Give the position of every Plasmodium parasite.
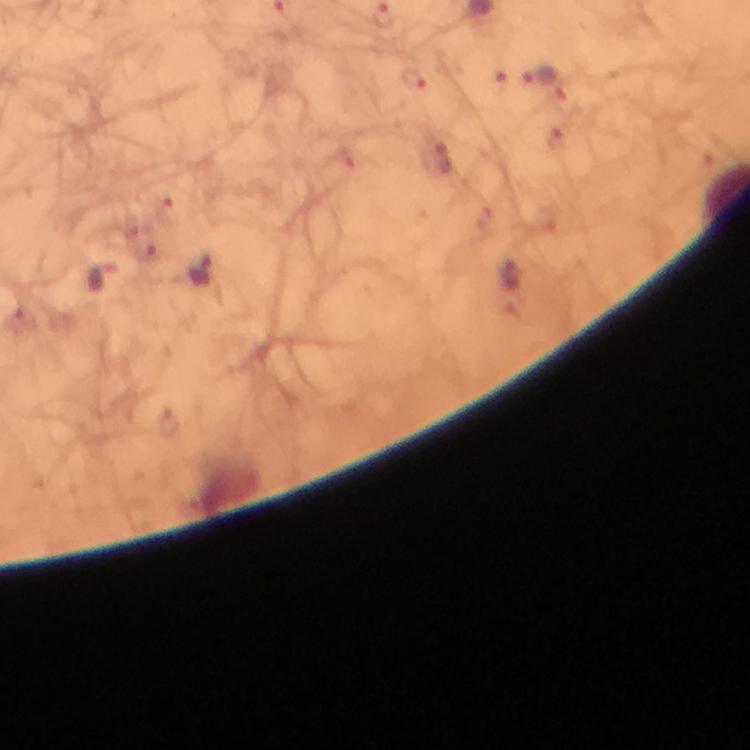
Approximate object centers, in pixels from the top-left corner.
Plasmodium parasites: (x=541, y=77), (x=413, y=80), (x=203, y=272), (x=103, y=276).

Summary:
  - Image size: 750×750 pixels
  - Stain: Giemsa
  - Context: from a malaria diagnostic workup
  - Preparation: thick blood smear
  - Magnification: 100x
  - Cropped from: one field of view
  - Capture: smartphone photograph through a microscope
  - Immersion oil: applied